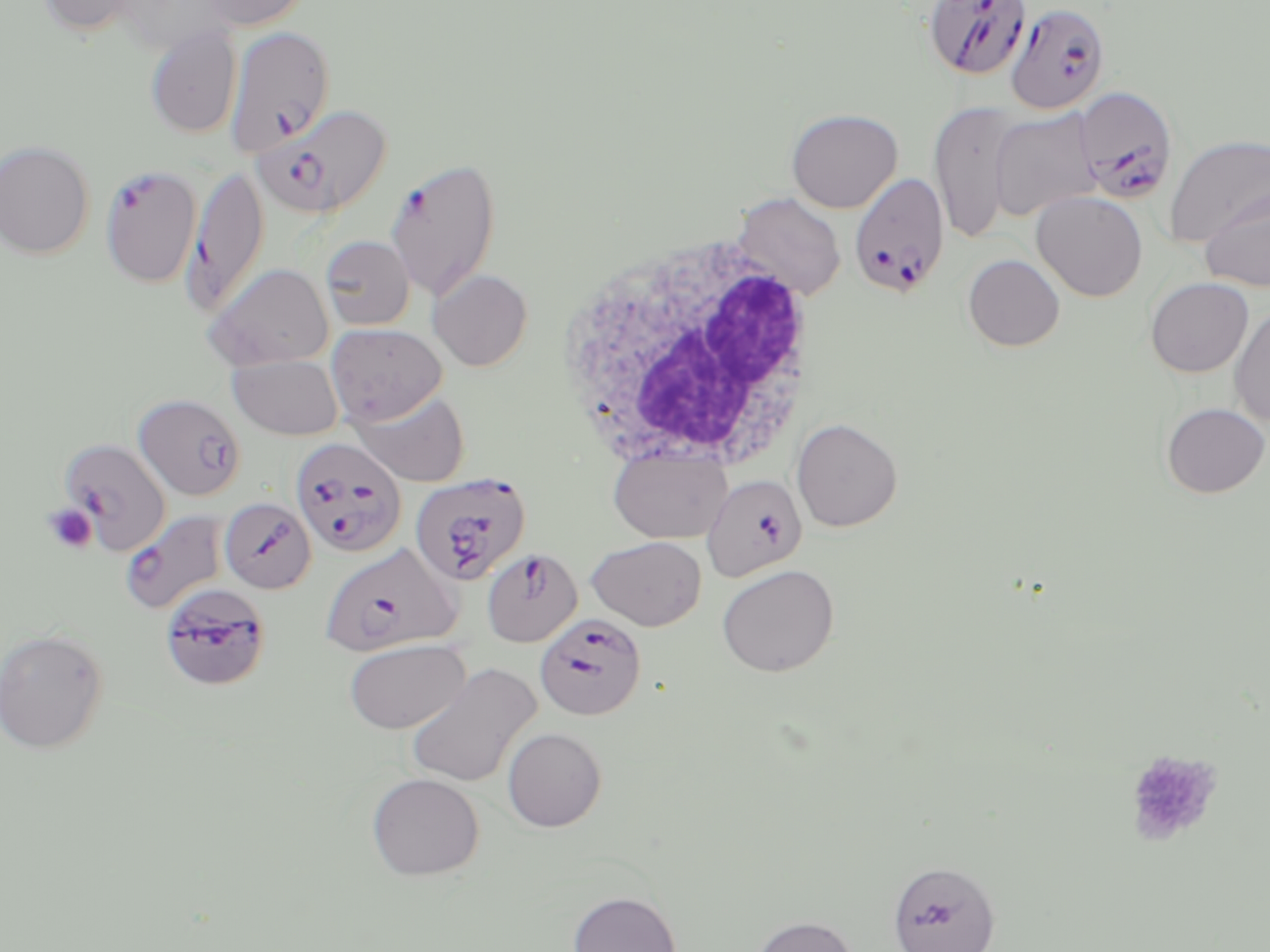
slide_level_diagnosis: Plasmodium falciparum
magnification: 1000x
field_of_view: single
preparation: thin blood smear
plasmodium_falciparum_infected_red_blood_cell_locations: 'approximate bounding boxes as (x1,y1)-(x2,y2) corner pairs in pixels: (924,0)-(1033,81), (1004,2)-(1110,114), (225,26)-(334,155), (1073,86)-(1179,205), (254,103)-(393,218), (386,157)-(502,300), (100,164)-(202,288), (184,165)-(268,316), (848,173)-(948,299), (134,393)-(246,501), (291,436)-(407,558), (60,438)-(171,555), (410,473)-(531,585), (701,474)-(807,581), (219,498)-(316,594), (120,511)-(230,615), (320,542)-(460,656), (481,548)-(582,646), (168,591)-(264,687), (535,612)-(646,720), (887,860)-(1000,952)'
white_blood_cell_locations: 'approximate bounding boxes as (x1,y1)-(x2,y2) corner pairs in pixels: (558,230)-(824,479)'
uninfected_red_blood_cell_locations: 'approximate bounding boxes as (x1,y1)-(x2,y2) corner pairs in pixels: (37,0)-(143,36), (196,0)-(312,31), (115,1)-(237,54), (145,26)-(242,138), (929,100)-(1021,246), (786,108)-(903,213), (989,109)-(1101,220), (1163,134)-(1270,247), (0,140)-(94,259), (1201,187)-(1269,291), (1031,191)-(1148,301), (731,192)-(846,302), (320,235)-(415,330), (963,254)-(1065,351), (203,262)-(334,370), (429,268)-(533,371), (1145,277)-(1253,377), (1229,306)-(1270,426), (326,323)-(447,425), (228,355)-(344,440), (350,390)-(470,486), (1161,402)-(1269,498), (791,417)-(903,532), (608,447)-(732,544), (587,536)-(706,630), (716,564)-(839,677), (0,629)-(109,754), (344,639)-(470,734), (407,663)-(541,787), (502,727)-(607,831), (366,772)-(484,880), (568,890)-(682,952), (750,915)-(858,952)'
platelet_locations: 'approximate bounding boxes as (x1,y1)-(x2,y2) corner pairs in pixels: (42,503)-(98,554), (1123,750)-(1223,846)'
image_size: 1270×952 pixels
modality: light microscopy
stain: May-Grünwald-Giemsa